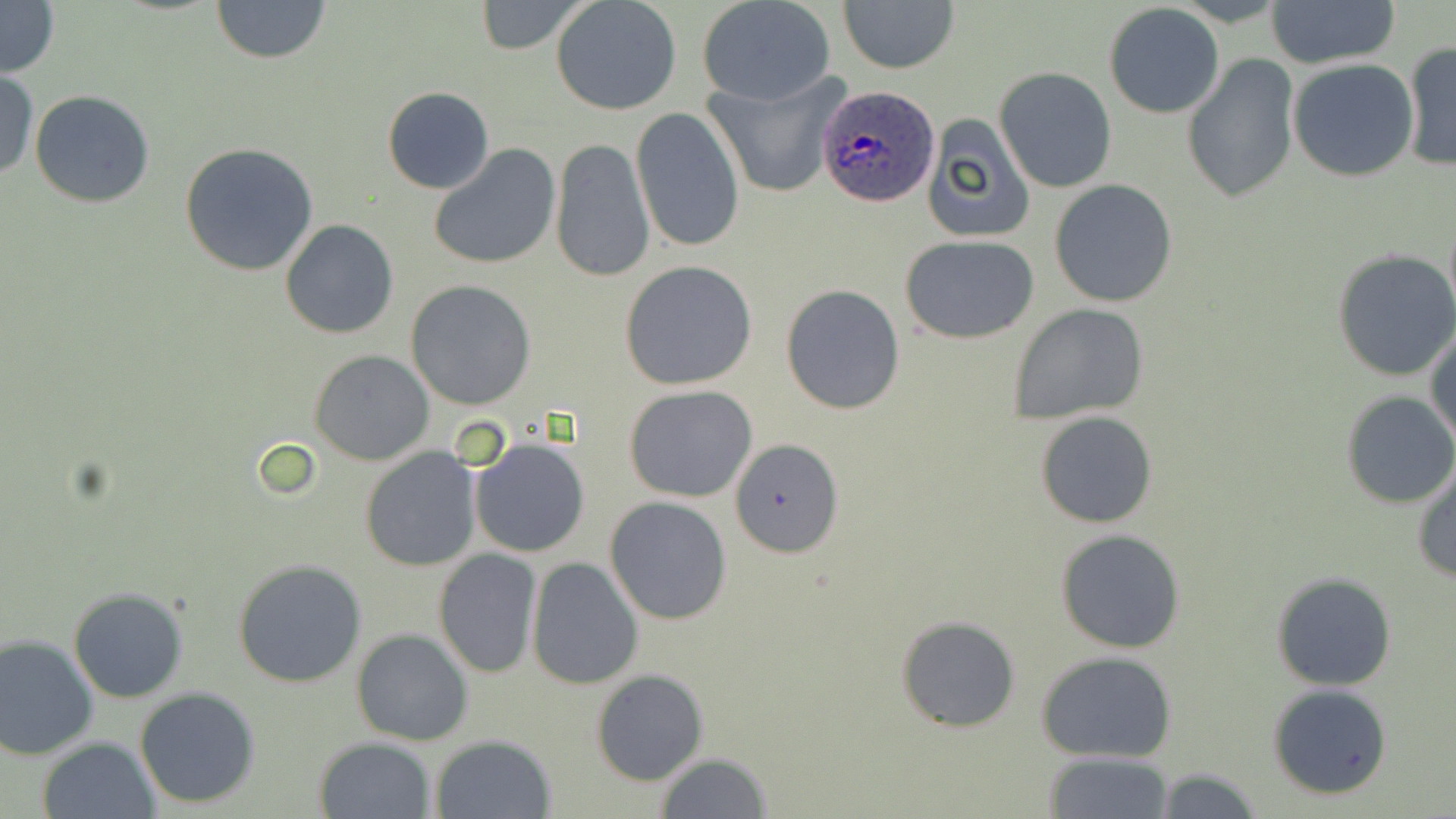

Approximate bounding boxes as (x1, y1, x2, y2) in pixels. Uninfected red blood cell locations: (210, 0, 330, 64), (551, 0, 682, 116), (698, 0, 837, 106), (0, 1, 59, 78), (472, 1, 589, 54), (839, 1, 959, 75), (1266, 1, 1400, 70), (1103, 4, 1225, 119), (1402, 41, 1455, 172), (1181, 54, 1299, 205), (1287, 57, 1418, 182), (995, 67, 1116, 193), (0, 72, 37, 181), (702, 72, 850, 200), (383, 86, 493, 193), (29, 90, 158, 208), (630, 106, 743, 256), (920, 113, 1038, 244), (549, 137, 654, 282), (179, 143, 319, 277), (429, 144, 561, 270), (1050, 180, 1178, 308), (280, 219, 399, 338), (900, 236, 1039, 343), (1332, 250, 1456, 379), (619, 260, 760, 392), (406, 280, 536, 410), (780, 284, 906, 415), (1009, 305, 1150, 424), (1426, 323, 1456, 451), (310, 349, 435, 464), (623, 383, 759, 501), (1342, 390, 1456, 509), (1035, 410, 1157, 528), (731, 436, 843, 558), (470, 438, 589, 558), (361, 447, 483, 571), (1412, 463, 1456, 585), (605, 495, 733, 624), (1054, 527, 1187, 653), (434, 548, 543, 679), (526, 556, 644, 689), (233, 559, 367, 687), (1270, 571, 1398, 691), (68, 587, 189, 703), (895, 613, 1021, 733), (352, 629, 474, 746), (0, 633, 99, 759), (1037, 650, 1180, 763), (590, 669, 706, 785), (1267, 683, 1393, 799), (135, 687, 260, 808), (431, 734, 555, 818), (37, 736, 160, 819), (315, 736, 435, 818), (1044, 750, 1175, 819), (654, 752, 774, 819), (1152, 766, 1265, 819). Plasmodium ovale-infected red blood cell locations: (818, 85, 943, 208). Slide-level diagnosis: Plasmodium ovale. Optical microscopy. Thin blood film. Image is 1456×819 pixels. Single field of view. May-Grünwald-Giemsa stain. 1000x magnification.